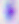
identification = Toxoplasma gondii
modality = photomicrograph
magnification = 400x